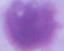
Summary:
  - Magnification: 1000x
  - Modality: photomicrograph
  - Identification: erythrocyte